Assess the morphology of the erythrocytes.
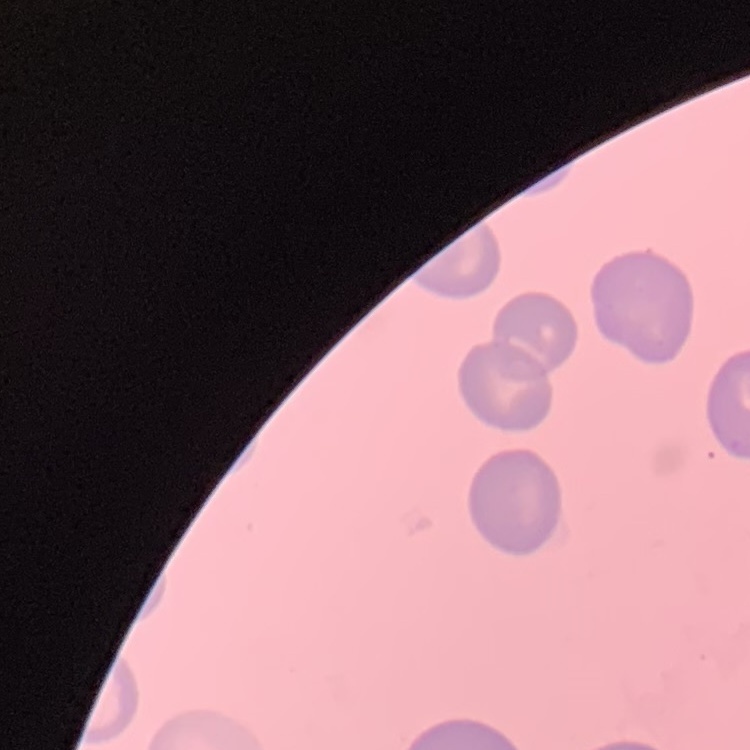
No rouleaux formation.

Summary:
  - Preparation: thin blood smear
  - Stain: Field's or Giemsa
  - Image type: square crop of a larger photomicrograph